Assess this cell for malaria.
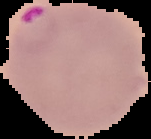

Parasitized.

Summary:
  - Preparation: thin blood smear
  - Image type: segmented cell region with the area outside set to black
  - Image size: 151×139 pixels